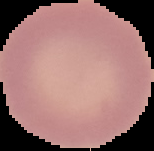
image_type: cell region segmented out of the field of view; surrounding area masked to black
malaria_status: uninfected
image_size: 154×151 pixels
preparation: thin blood smear